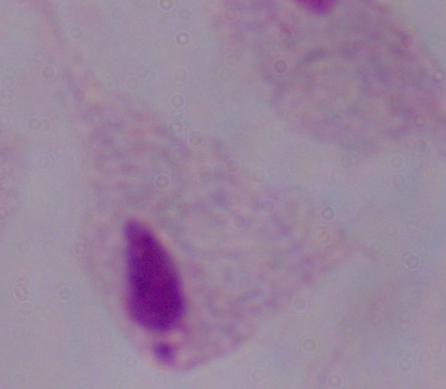 Micrograph. 1000x magnification. A trichomonad is shown.